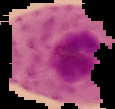

Summary:
  - Result: malaria parasites identified
  - Image type: segmented cell region on a black background
  - Image size: 115×109 pixels
  - Preparation: thin blood film